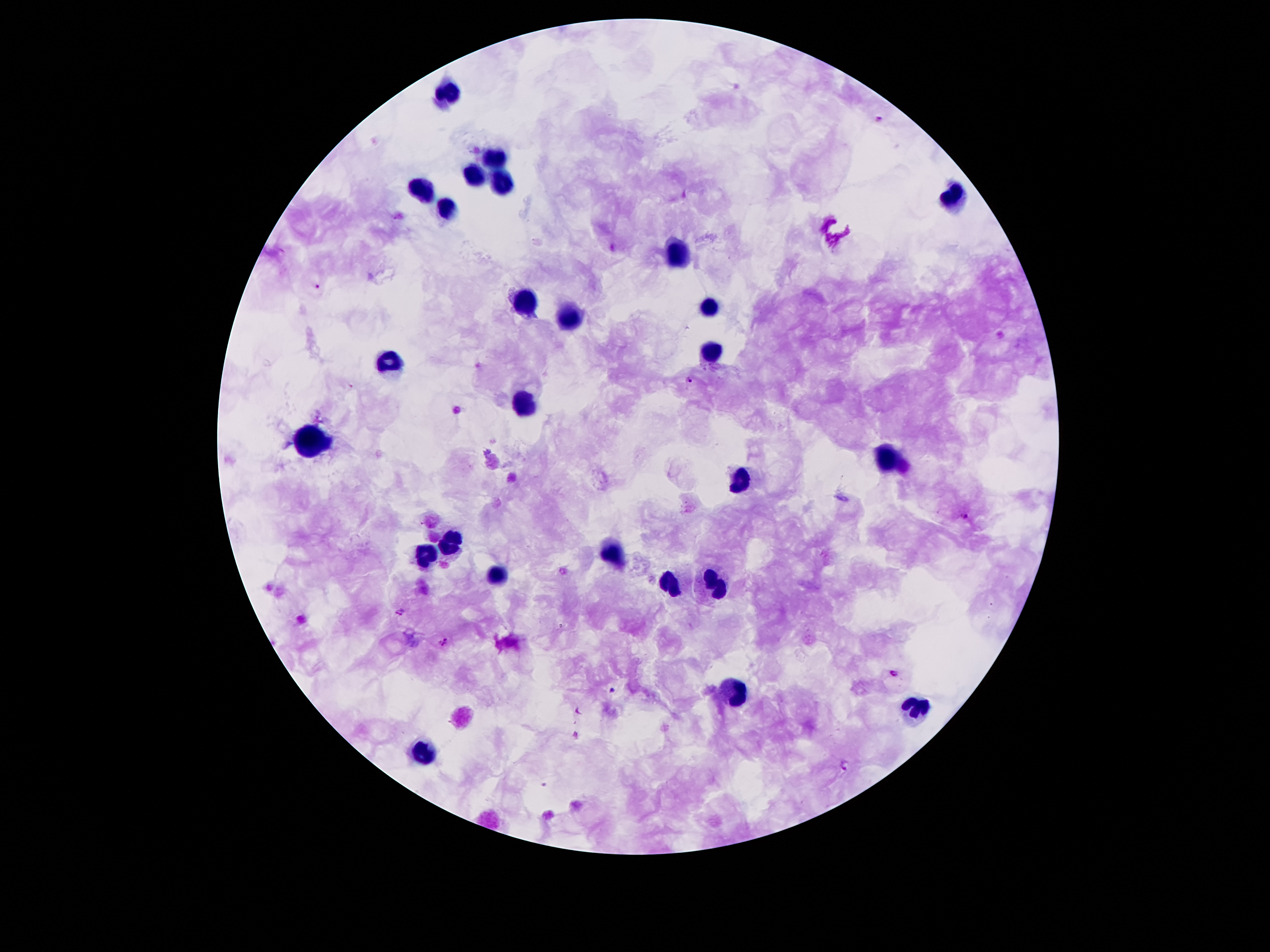
Approximate centers as {x, y} in pixels.
Summary:
  - Plasmodium parasite locations: {880, 119}, {317, 285}, {690, 381}, {966, 516}, {400, 612}, {445, 641}, {894, 673}, {612, 691}, {847, 764}
  - Leukocyte locations: {450, 91}, {497, 156}, {472, 177}, {503, 181}, {421, 188}, {952, 195}, {450, 207}, {679, 252}, {522, 303}, {708, 309}, {571, 315}, {710, 354}, {390, 361}, {522, 406}, {314, 441}, {886, 460}, {741, 480}, {450, 541}, {616, 555}, {427, 556}, {493, 577}, {671, 586}, {716, 586}, {737, 693}, {917, 707}, {424, 751}
  - Field of view: single
  - Patient malaria status: positive for Plasmodium falciparum
  - Preparation: thick blood film
  - Stain: Giemsa
  - Magnification: 100x
  - Image size: 1270×952 pixels
  - Capture: smartphone camera through the microscope eyepiece